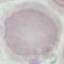

Result: no malaria parasites seen. Photographed with a smartphone camera at the microscope eyepiece. Giemsa stain. Thin blood smear. Automatically extracted cell patch, resized to 64 × 64 pixels.